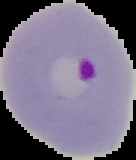 Image is 136×160 pixels. Segmented cell region on a black background. Malaria status: parasitized. From a thin blood smear.